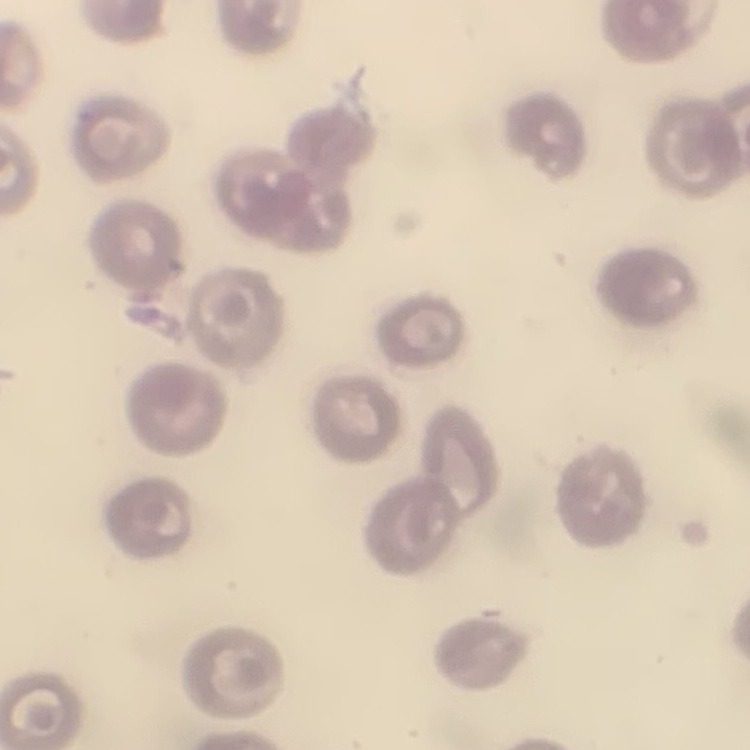 The erythrocytes show no rouleaux formation. Field's or Giemsa stain. One tile cut from a larger photomicrograph. Thin blood film.